Comment on the morphology of the erythrocytes.
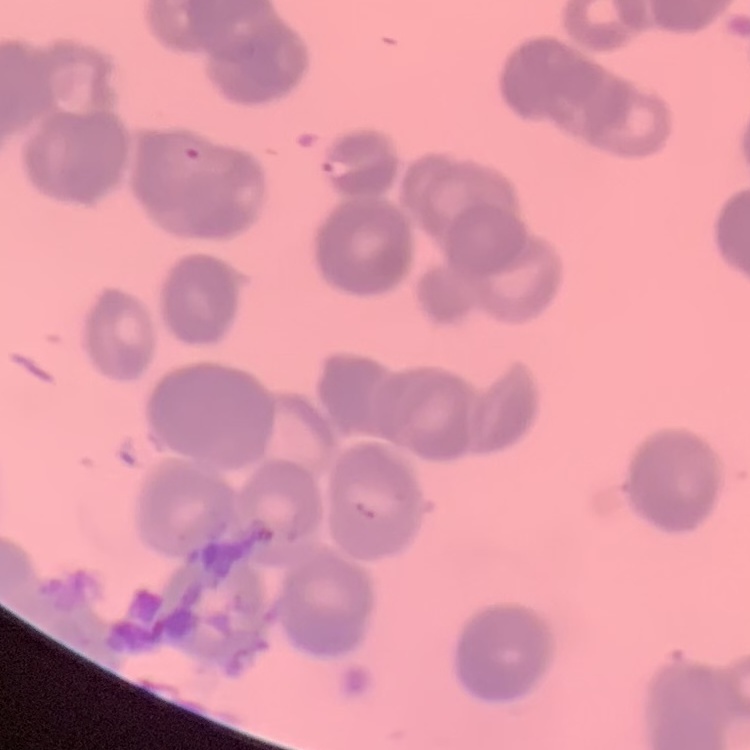
They show rouleaux formation.

preparation = thin peripheral smear
stain = Field's or Giemsa
image type = one tile cut from a larger photomicrograph